Classify this cell by malaria status.
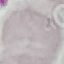
Uninfected.

Summary:
  - Capture: smartphone camera at the microscope eyepiece
  - Preparation: thin blood smear
  - Stain: Giemsa
  - Image type: automatically extracted cell patch, resized to 64 × 64 pixels